Classify this cell by malaria status.
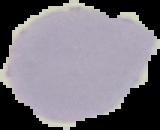
It is uninfected.

image type = segmented cell region on a black background
image size = 160×130 pixels
preparation = thin blood smear